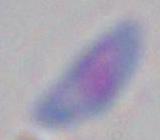
modality = photomicrograph
identification = Toxoplasma gondii
magnification = 1000x